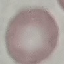

Summary:
  - Result: no malaria parasites seen
  - Image type: automatically extracted cell patch, resized to 64 × 64 pixels
  - Preparation: thin blood film
  - Stain: Giemsa
  - Capture: smartphone camera at the microscope eyepiece